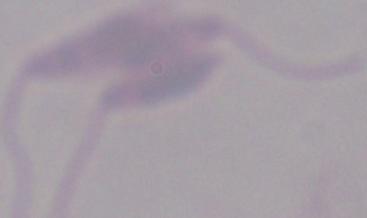

magnification = 1000x
identification = Leishmania
modality = photomicrograph